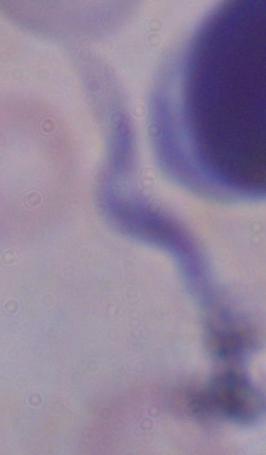

modality = micrograph
magnification = 1000x
identification = trypanosome